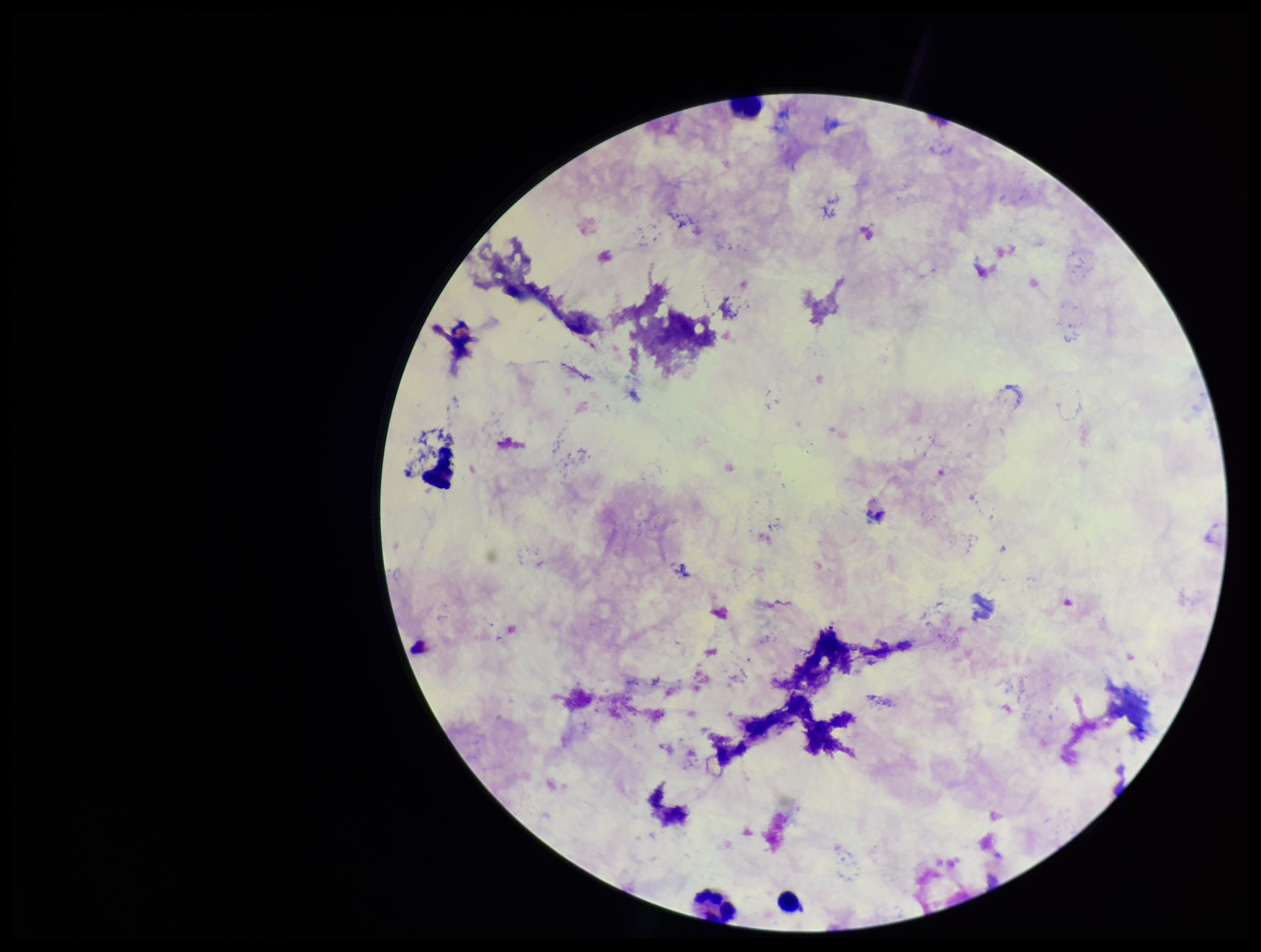
Photographed through the microscope eyepiece with a smartphone camera. Preparation: thick. Plasmodium parasites: none identified. One field from this slide. Leukocyte count: 3. Patient malaria status: negative. Giemsa stain. Parasite count: 0. Image is 1261×952 pixels.